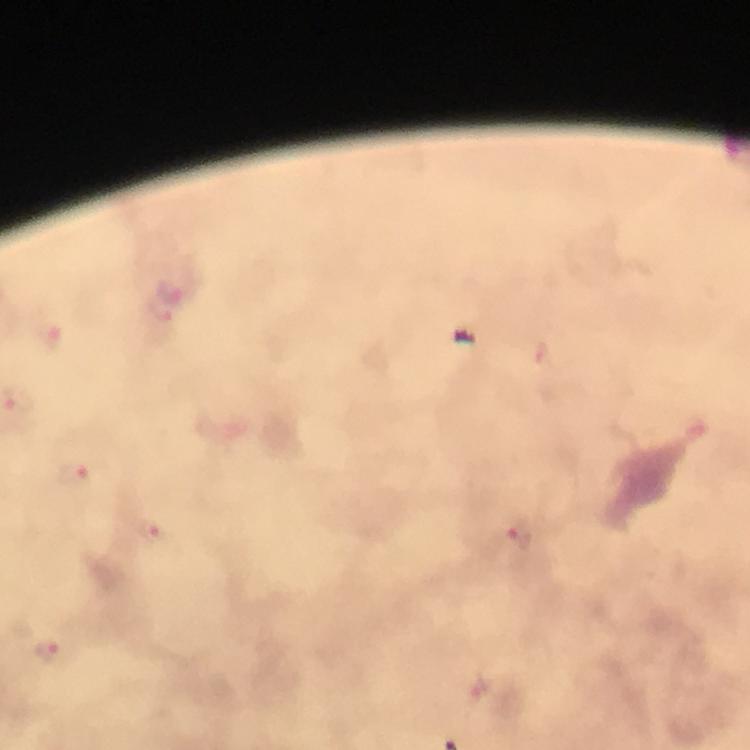 Approximate centers as (x, y) in pixels. Malaria parasite locations: (172, 295), (51, 336), (74, 471), (518, 533), (157, 536), (47, 652). Immersion oil applied. Cropped region of a single field of view. At 100x magnification. Photographed with a smartphone mounted on the microscope. Giemsa stain. From a malaria diagnostic workup. Image is 750×750 pixels. Thick smear.